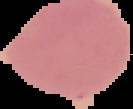

Summary:
  - Image size: 133×109 pixels
  - Malaria status: uninfected
  - Preparation: thin blood smear
  - Image type: segmented cell region on a black background